Classify this cell by malaria status.
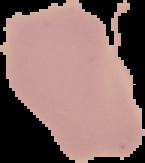

Uninfected.

image type = segmented cell region on a black background
preparation = thin blood film
image size = 145×163 pixels